Locate every leukocyte (white blood cell).
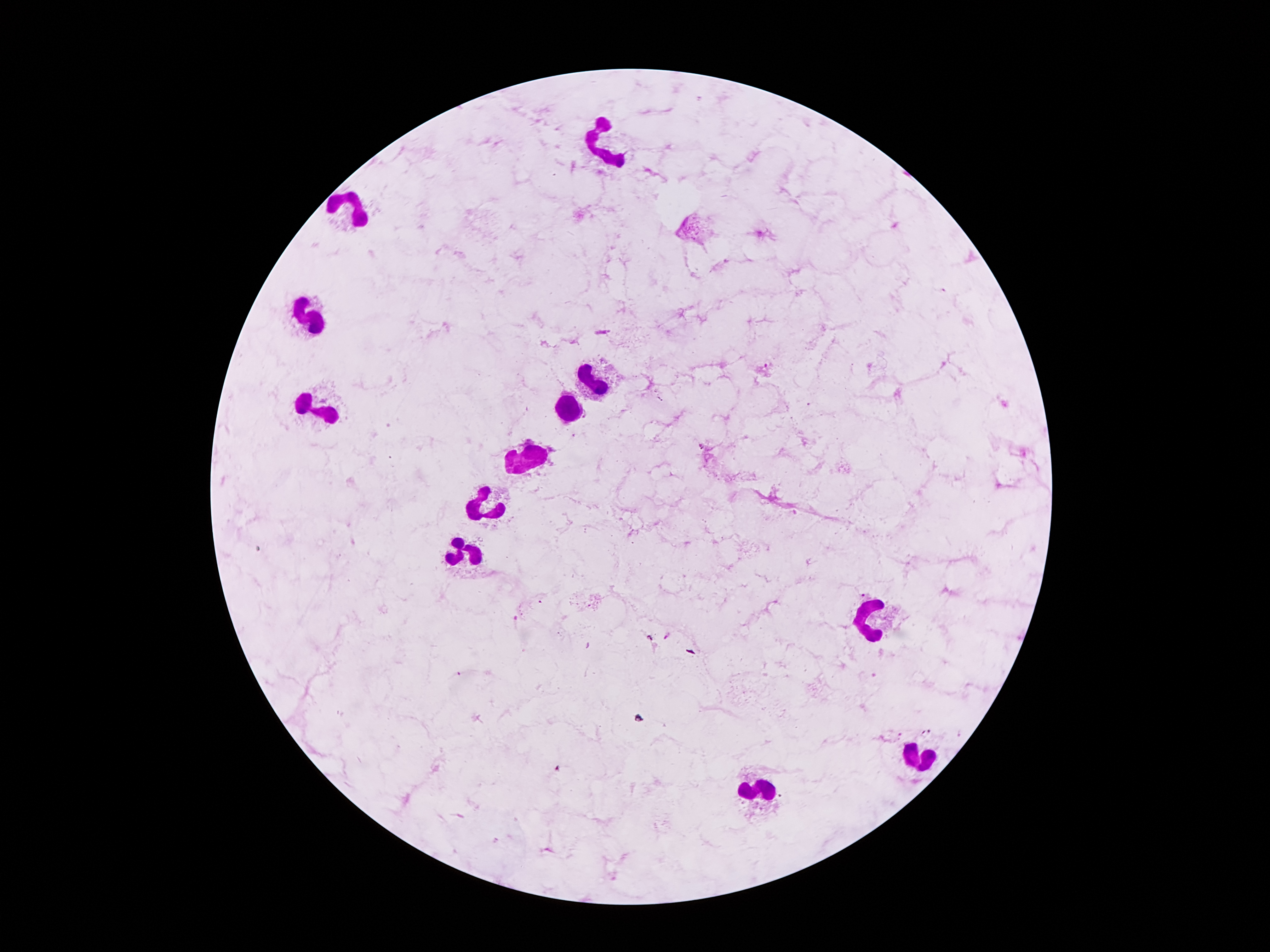
Approximate centers as {x, y} in pixels.
Leukocytes: {609, 145}, {352, 203}, {315, 320}, {592, 381}, {323, 412}, {568, 414}, {531, 458}, {488, 507}, {463, 559}, {864, 621}, {915, 756}, {760, 792}.

{
  "patient_malaria_status": "positive for Plasmodium falciparum",
  "magnification": "100x",
  "image_size": "1270×952 pixels",
  "capture": "smartphone camera through the microscope eyepiece",
  "field_of_view": "one from this slide",
  "stain": "Giemsa",
  "plasmodium_parasite_locations": "approximate centers as {x, y} in pixels: {766, 366}, {586, 415}, {701, 446}, {863, 595}, {516, 618}, {668, 637}, {876, 673}",
  "preparation": "thick blood smear"
}